Give the extent of all uninfected red blood cells.
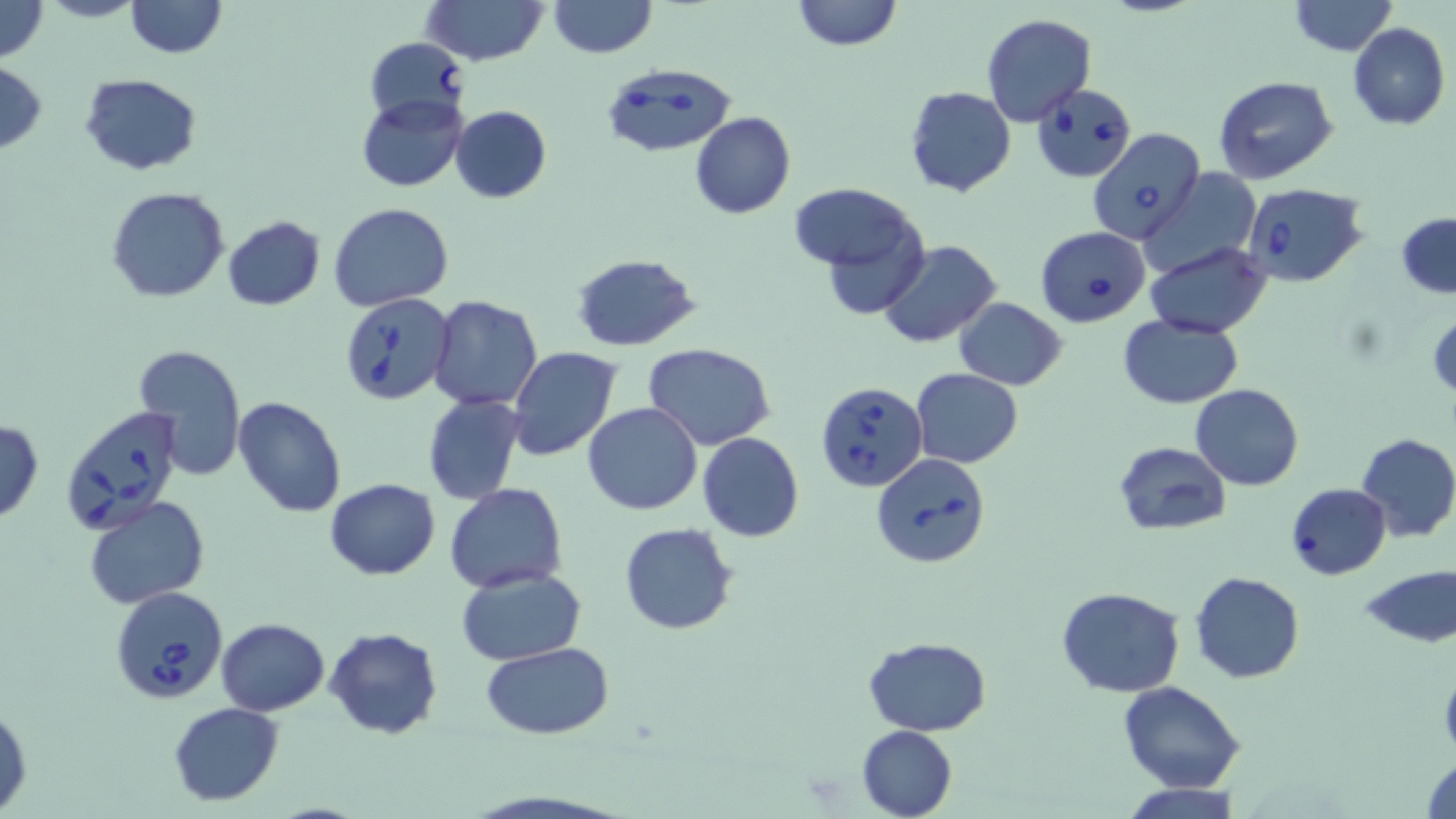
Approximate bounding boxes as named x1/y1/x2/y2 corners in pixels.
Uninfected red blood cells: (x1=0, y1=0, x2=49, y2=63), (x1=37, y1=0, x2=147, y2=23), (x1=123, y1=0, x2=227, y2=58), (x1=421, y1=0, x2=547, y2=67), (x1=549, y1=0, x2=655, y2=57), (x1=791, y1=0, x2=902, y2=52), (x1=1288, y1=1, x2=1397, y2=55), (x1=981, y1=14, x2=1098, y2=127), (x1=1346, y1=23, x2=1450, y2=130), (x1=0, y1=62, x2=47, y2=152), (x1=80, y1=73, x2=202, y2=175), (x1=1213, y1=76, x2=1339, y2=187), (x1=904, y1=86, x2=1016, y2=198), (x1=356, y1=93, x2=468, y2=192), (x1=449, y1=105, x2=552, y2=203), (x1=690, y1=111, x2=795, y2=219), (x1=1142, y1=166, x2=1262, y2=277), (x1=788, y1=183, x2=920, y2=275), (x1=105, y1=187, x2=230, y2=303), (x1=329, y1=202, x2=454, y2=310), (x1=1398, y1=213, x2=1456, y2=299), (x1=221, y1=215, x2=326, y2=311), (x1=876, y1=238, x2=1003, y2=349), (x1=1144, y1=244, x2=1273, y2=337), (x1=571, y1=252, x2=702, y2=349), (x1=427, y1=294, x2=543, y2=410), (x1=953, y1=298, x2=1068, y2=390), (x1=1427, y1=310, x2=1456, y2=401), (x1=1118, y1=314, x2=1242, y2=409), (x1=645, y1=344, x2=776, y2=451), (x1=132, y1=345, x2=247, y2=481), (x1=507, y1=347, x2=623, y2=462), (x1=910, y1=368, x2=1024, y2=468), (x1=1191, y1=383, x2=1304, y2=490), (x1=423, y1=394, x2=526, y2=505), (x1=233, y1=395, x2=346, y2=517), (x1=582, y1=402, x2=704, y2=515), (x1=1, y1=418, x2=45, y2=523), (x1=697, y1=432, x2=803, y2=543), (x1=1356, y1=433, x2=1456, y2=541), (x1=1113, y1=440, x2=1232, y2=536), (x1=324, y1=478, x2=440, y2=580), (x1=1286, y1=483, x2=1390, y2=579), (x1=443, y1=484, x2=568, y2=594), (x1=83, y1=495, x2=209, y2=609), (x1=619, y1=523, x2=739, y2=635), (x1=1359, y1=565, x2=1456, y2=648), (x1=457, y1=569, x2=584, y2=665), (x1=1190, y1=571, x2=1304, y2=683), (x1=1057, y1=587, x2=1186, y2=697), (x1=216, y1=617, x2=330, y2=714), (x1=324, y1=626, x2=444, y2=740), (x1=864, y1=636, x2=989, y2=737), (x1=482, y1=644, x2=615, y2=739), (x1=1117, y1=681, x2=1247, y2=793), (x1=168, y1=702, x2=284, y2=805), (x1=1, y1=703, x2=32, y2=816), (x1=857, y1=724, x2=956, y2=819), (x1=1422, y1=755, x2=1455, y2=818), (x1=1118, y1=783, x2=1247, y2=818).

slide-level diagnosis = Babesia divergens
modality = optical microscopy
preparation = thin blood smear
image size = 1456×819 pixels
field of view = single
Babesia divergens-infected red blood cell locations = approximate bounding boxes as named x1/y1/x2/y2 corners in pixels: (x1=363, y1=38, x2=469, y2=126), (x1=600, y1=64, x2=738, y2=158), (x1=1030, y1=84, x2=1138, y2=182), (x1=1088, y1=127, x2=1206, y2=244), (x1=1241, y1=181, x2=1369, y2=286), (x1=1033, y1=225, x2=1151, y2=328), (x1=338, y1=291, x2=454, y2=408), (x1=815, y1=380, x2=927, y2=492), (x1=59, y1=403, x2=187, y2=537), (x1=872, y1=453, x2=992, y2=570), (x1=110, y1=584, x2=229, y2=705)
stain = May-Grünwald-Giemsa
magnification = 1000x